Point out each Plasmodium parasite.
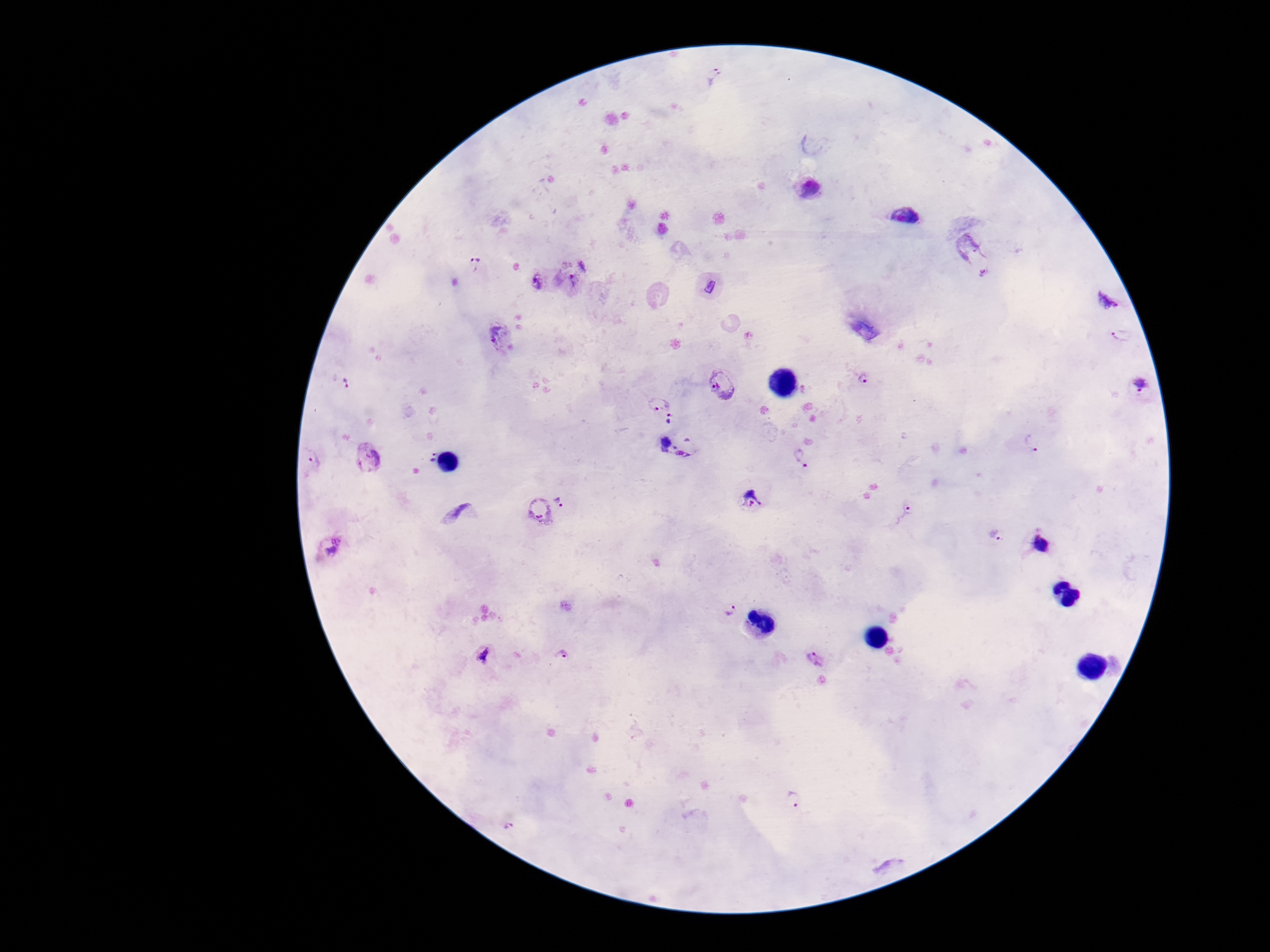
Approximate centers as [x, y] in pixels.
Plasmodium parasites: [584, 263], [475, 264], [535, 281], [574, 282], [1107, 296], [501, 334], [1121, 334], [865, 380], [724, 382], [346, 384], [1142, 385], [657, 401], [676, 419], [1034, 444], [674, 454], [366, 458], [803, 458], [313, 462], [565, 496], [751, 502], [538, 509], [905, 513], [997, 536], [1040, 544], [335, 548], [728, 607], [485, 654], [564, 656], [815, 658], [793, 797], [510, 825].

Summary:
  - Image size: 1270×952 pixels
  - Preparation: thick peripheral-blood smear
  - Field of view: single
  - Patient malaria status: infected
  - Magnification: 100x
  - Stain: Giemsa
  - Capture: smartphone camera through the microscope eyepiece